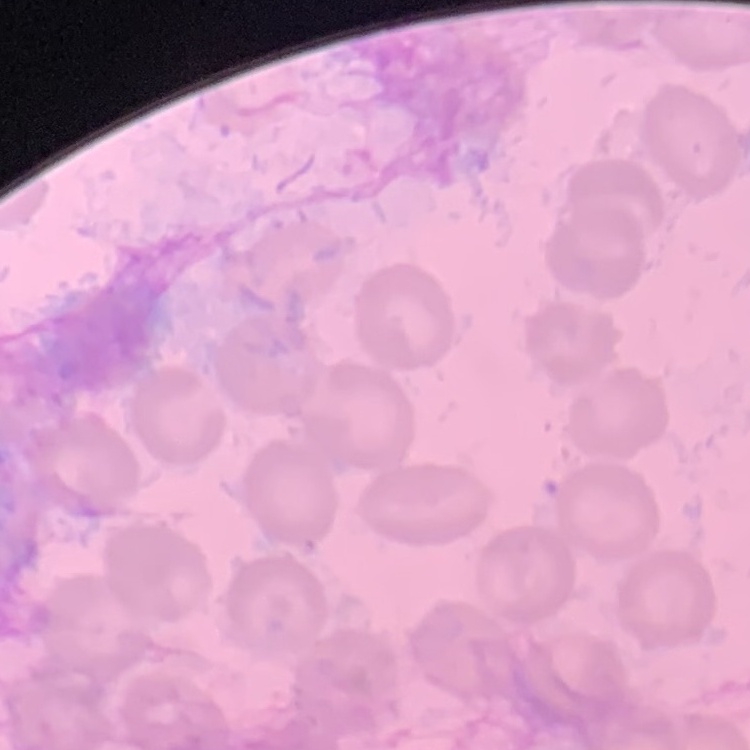
The erythrocytes show no rouleaux formation. Thin peripheral smear. Stained with either Field's or Giemsa. One tile cut from a larger photomicrograph.